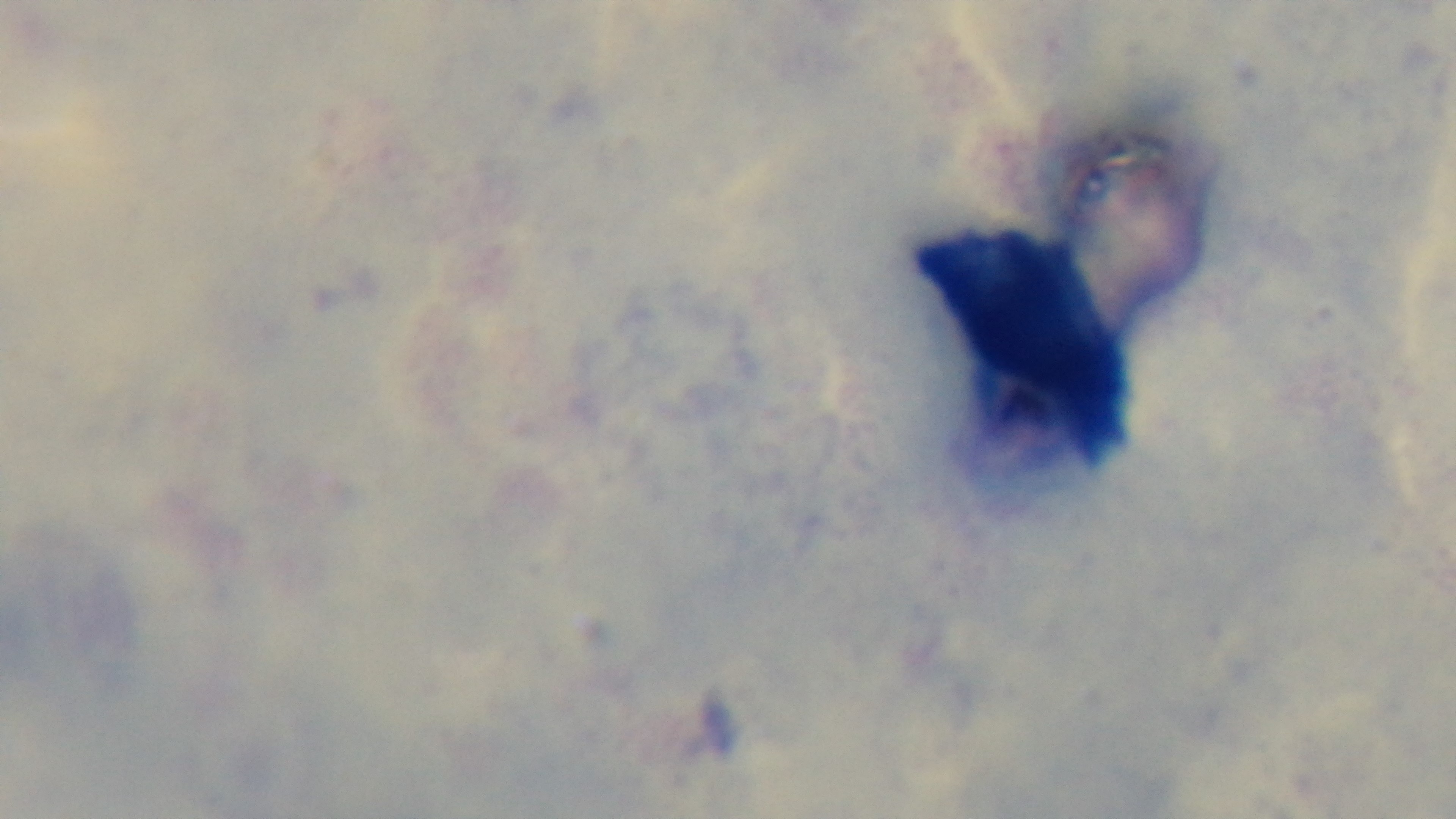

Captured with a mounted 4K digital camera. Photomicrograph. Giemsa-stained. Preparation: thick. Malaria status: negative. Single field of view. Oil-immersion objective, 100x.